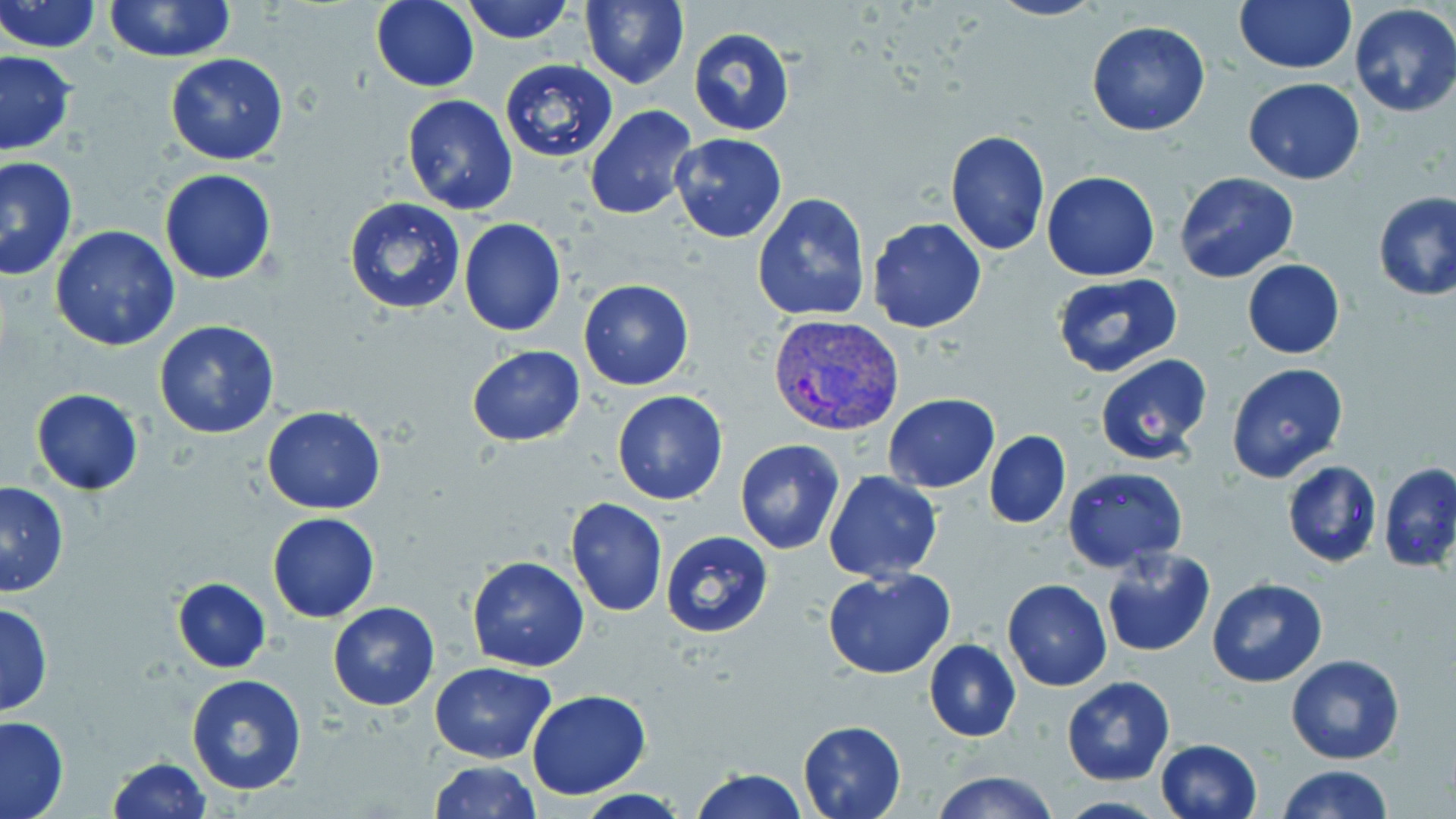
Summary:
  - Coordinate format: approximate bounding boxes as [x1, y1, x2, y2] in pixels
  - Uninfected red blood cell locations: [0, 0, 103, 53], [370, 0, 478, 92], [459, 0, 577, 45], [986, 0, 1106, 23], [1233, 0, 1357, 73], [102, 1, 237, 62], [579, 1, 690, 88], [1349, 3, 1456, 117], [1086, 21, 1211, 137], [689, 28, 795, 135], [0, 50, 76, 158], [165, 52, 289, 165], [499, 58, 617, 163], [1243, 78, 1366, 184], [401, 94, 518, 215], [585, 104, 698, 221], [945, 129, 1050, 255], [670, 132, 788, 243], [0, 157, 78, 283], [159, 168, 278, 284], [1041, 171, 1160, 280], [1174, 172, 1300, 282], [1373, 191, 1456, 301], [753, 194, 872, 321], [344, 197, 466, 314], [459, 218, 567, 337], [866, 218, 988, 334], [49, 226, 180, 350], [1241, 259, 1345, 359], [1052, 273, 1184, 379], [578, 280, 693, 390], [153, 319, 280, 439], [466, 344, 587, 447], [1095, 355, 1213, 465], [1226, 362, 1348, 485], [30, 389, 142, 494], [612, 390, 728, 505], [883, 394, 1000, 491], [262, 407, 386, 513], [985, 430, 1070, 528], [735, 439, 845, 554], [1282, 460, 1381, 568], [1379, 462, 1456, 573], [1061, 467, 1186, 572], [823, 471, 943, 583], [0, 482, 70, 597], [565, 498, 668, 616], [267, 512, 380, 623], [659, 530, 774, 638], [1101, 547, 1215, 658], [466, 556, 591, 672], [822, 566, 956, 679], [172, 577, 270, 671], [1003, 578, 1111, 690], [1207, 578, 1327, 687], [0, 600, 53, 715], [328, 602, 440, 711], [923, 638, 1020, 741], [1286, 653, 1405, 765], [431, 662, 558, 762], [185, 672, 307, 795], [1062, 676, 1175, 786], [527, 689, 651, 799], [0, 714, 70, 818], [797, 720, 905, 819], [1155, 738, 1263, 819], [107, 758, 211, 818], [429, 760, 540, 818], [1276, 764, 1394, 819], [690, 767, 807, 819], [933, 770, 1059, 819], [574, 790, 689, 819], [1055, 795, 1169, 818]
  - Plasmodium vivax-infected red blood cell locations: [769, 314, 904, 439]
  - Slide-level diagnosis: Plasmodium vivax
  - Modality: optical microscopy
  - Magnification: 1000x
  - Stain: May-Grünwald-Giemsa
  - Image size: 1456×819 pixels
  - Field of view: one of a larger specimen
  - Preparation: thin blood smear